Describe the morphology of the red blood cells.
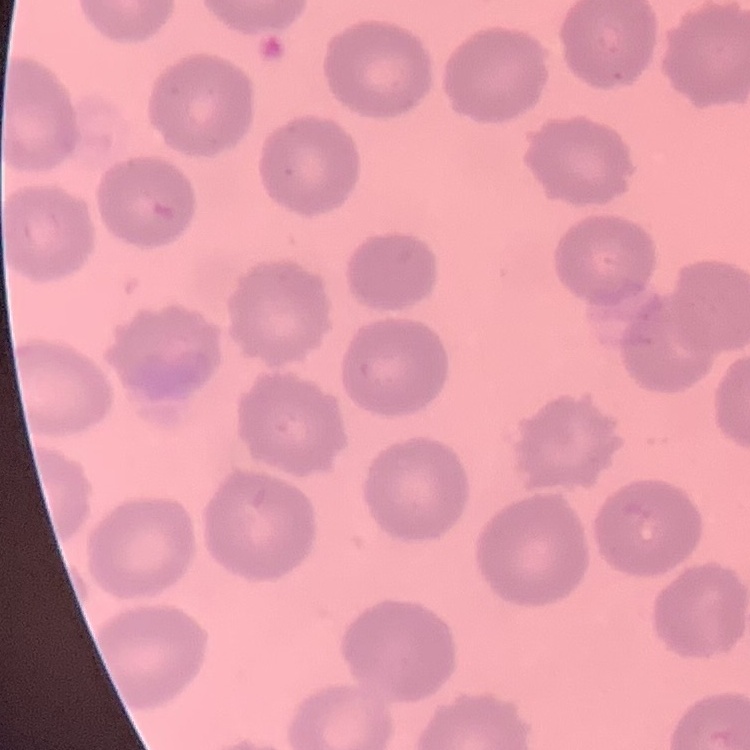
No rouleaux formation.

Thin peripheral smear. Square crop of a larger photomicrograph. Stained with either Field's or Giemsa.